Assess this cell for malaria.
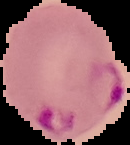
Parasitized.

Summary:
  - Preparation: thin blood smear
  - Image type: cell region segmented out of the field of view; surrounding area masked to black
  - Image size: 130×145 pixels